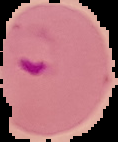
image size = 118×142 pixels
image type = segmented cell region on a black background
preparation = thin blood film
malaria status = parasitized